Locate every Plasmodium parasite and identify its life-cycle stage.
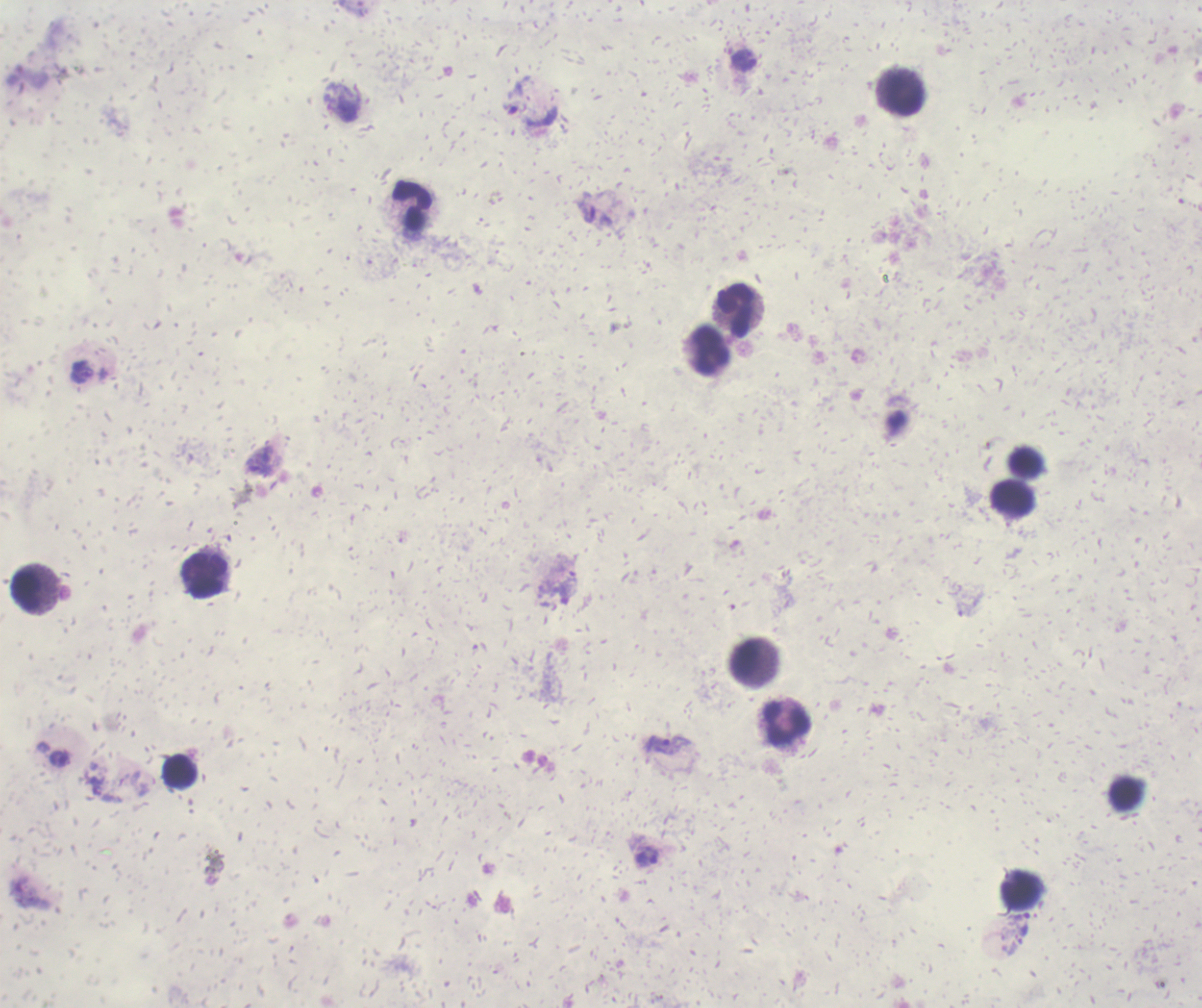
Approximate centers as [x, y] in pixels.
Trophozoites: [533, 115], [82, 372], [259, 461], [668, 744], [647, 857], [1023, 923].
No schizont or gametocyte forms observed.

Approximate centers as [x, y] in pixels. Leukocyte locations: [900, 93], [413, 207], [736, 311], [709, 350], [1025, 462], [1012, 498], [206, 576], [26, 592], [745, 657], [787, 724], [180, 771], [1125, 795], [1021, 890]. Thick blood smear. Image is 1202×1008 pixels. Coloration quality: bad. Captured at 100x magnification. Background quality: unsatisfactory. Romanowsky stain. Single field of view. Previously used in an actual diagnosis.